Assess this cell for malaria.
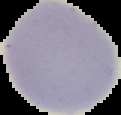

It is uninfected.

image_type: segmented cell region on a black background
image_size: 121×115 pixels
preparation: thin blood smear